Locate every blood parasite and identify its species.
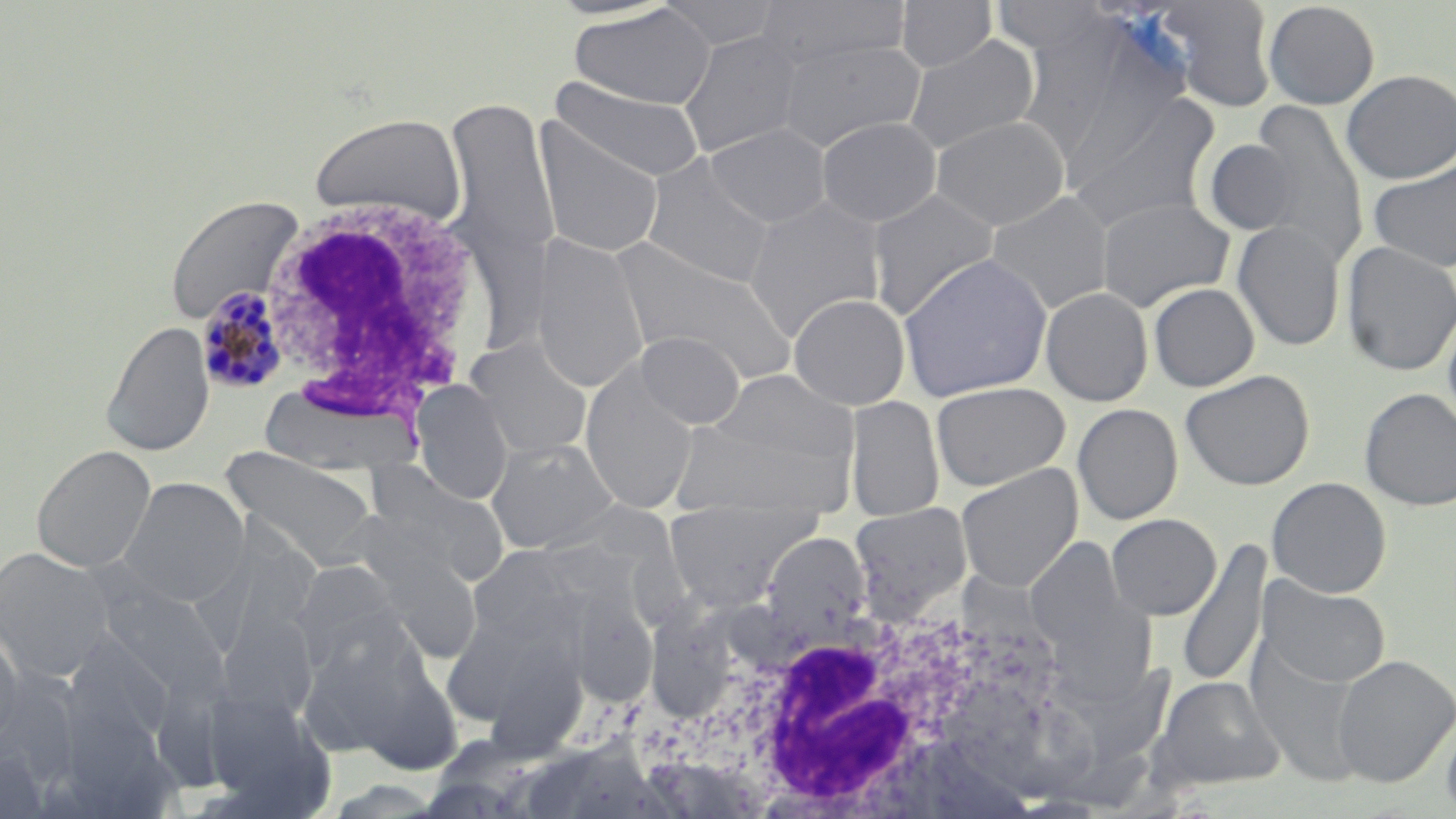

Approximate bounding boxes as named x1/y1/x2/y2 corners in pixels.
Plasmodium malariae-infected red blood cells: (x1=195, y1=284, x2=292, y2=396).
No Plasmodium falciparum, Plasmodium ovale, Plasmodium vivax, Babesia divergens, or Trypanosoma brucei observed.

slide-level diagnosis = Plasmodium malariae
preparation = thin blood smear
modality = optical microscopy
uninfected red blood cell locations = approximate bounding boxes as named x1/y1/x2/y2 corners in pixels: (x1=655, y1=0, x2=785, y2=52), (x1=754, y1=0, x2=913, y2=68), (x1=895, y1=0, x2=997, y2=72), (x1=990, y1=0, x2=1112, y2=56), (x1=1157, y1=1, x2=1279, y2=112), (x1=1263, y1=1, x2=1380, y2=109), (x1=569, y1=4, x2=716, y2=110), (x1=677, y1=31, x2=807, y2=158), (x1=1063, y1=34, x2=1192, y2=192), (x1=903, y1=35, x2=1040, y2=156), (x1=775, y1=37, x2=926, y2=152), (x1=1341, y1=69, x2=1456, y2=183), (x1=552, y1=78, x2=705, y2=182), (x1=1066, y1=91, x2=1221, y2=234), (x1=443, y1=98, x2=559, y2=268), (x1=1246, y1=101, x2=1368, y2=271), (x1=308, y1=112, x2=467, y2=227), (x1=930, y1=115, x2=1070, y2=232), (x1=816, y1=117, x2=941, y2=227), (x1=532, y1=120, x2=666, y2=260), (x1=705, y1=123, x2=831, y2=228), (x1=1203, y1=139, x2=1298, y2=235), (x1=641, y1=154, x2=778, y2=289), (x1=1368, y1=161, x2=1456, y2=273), (x1=867, y1=188, x2=1001, y2=321), (x1=985, y1=191, x2=1114, y2=314), (x1=164, y1=194, x2=305, y2=325), (x1=1096, y1=197, x2=1234, y2=311), (x1=743, y1=198, x2=886, y2=342), (x1=1231, y1=221, x2=1346, y2=352), (x1=529, y1=233, x2=649, y2=394), (x1=607, y1=237, x2=800, y2=385), (x1=1341, y1=241, x2=1456, y2=376), (x1=897, y1=253, x2=1053, y2=402), (x1=1148, y1=282, x2=1260, y2=392), (x1=1040, y1=287, x2=1153, y2=407), (x1=788, y1=294, x2=910, y2=410), (x1=1442, y1=304, x2=1456, y2=439), (x1=101, y1=321, x2=215, y2=456), (x1=634, y1=331, x2=745, y2=429), (x1=465, y1=336, x2=593, y2=461), (x1=581, y1=362, x2=699, y2=515), (x1=710, y1=368, x2=856, y2=472), (x1=1180, y1=369, x2=1315, y2=491), (x1=412, y1=381, x2=513, y2=504), (x1=931, y1=381, x2=1071, y2=491), (x1=258, y1=383, x2=424, y2=476), (x1=1359, y1=389, x2=1456, y2=510), (x1=845, y1=395, x2=945, y2=521), (x1=1072, y1=403, x2=1183, y2=525), (x1=671, y1=417, x2=846, y2=517), (x1=485, y1=437, x2=620, y2=554), (x1=31, y1=444, x2=156, y2=573), (x1=222, y1=447, x2=379, y2=565), (x1=360, y1=462, x2=511, y2=588), (x1=956, y1=463, x2=1083, y2=592), (x1=118, y1=477, x2=249, y2=606), (x1=1266, y1=477, x2=1391, y2=598), (x1=663, y1=501, x2=821, y2=609), (x1=849, y1=502, x2=973, y2=622), (x1=1105, y1=513, x2=1221, y2=620), (x1=760, y1=532, x2=871, y2=637), (x1=1026, y1=538, x2=1131, y2=655), (x1=1178, y1=540, x2=1271, y2=689), (x1=469, y1=545, x2=586, y2=646), (x1=0, y1=547, x2=115, y2=683), (x1=363, y1=549, x2=482, y2=665), (x1=290, y1=560, x2=414, y2=680), (x1=1257, y1=575, x2=1391, y2=689), (x1=95, y1=580, x2=229, y2=701), (x1=567, y1=591, x2=658, y2=708), (x1=1059, y1=601, x2=1154, y2=703), (x1=216, y1=612, x2=318, y2=724), (x1=0, y1=628, x2=27, y2=753), (x1=299, y1=631, x2=429, y2=756), (x1=61, y1=634, x2=177, y2=751), (x1=479, y1=639, x2=589, y2=761), (x1=1245, y1=640, x2=1368, y2=784), (x1=1332, y1=654, x2=1456, y2=787), (x1=348, y1=655, x2=463, y2=775), (x1=1074, y1=663, x2=1176, y2=758), (x1=0, y1=675, x2=84, y2=791), (x1=1150, y1=676, x2=1285, y2=791), (x1=198, y1=689, x2=329, y2=808), (x1=1440, y1=710, x2=1456, y2=818), (x1=0, y1=747, x2=50, y2=819)
stain = May-Grünwald-Giemsa
image size = 1456×819 pixels
field of view = one of a larger specimen
magnification = 1000x
white blood cell locations = approximate bounding boxes as named x1/y1/x2/y2 corners in pixels: (x1=255, y1=193, x2=492, y2=423), (x1=668, y1=591, x2=1017, y2=818)